Report the malaria status of this cell.
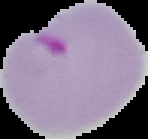
Parasitized.

{
  "image_size": "148×139 pixels",
  "preparation": "thin blood smear",
  "image_type": "segmented cell region on a black background"
}